Assess this cell for malaria.
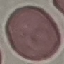
Uninfected.

Giemsa stain. Thin blood smear. Cell patch, automatically extracted from a larger field of view and resized to 64 × 64 pixels. Photographed with a smartphone camera at the microscope eyepiece.